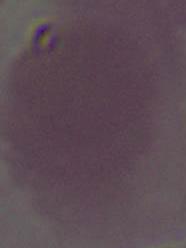

Micrograph. 1000x magnification. An erythrocyte is seen.